Look for Plasmodium parasites.
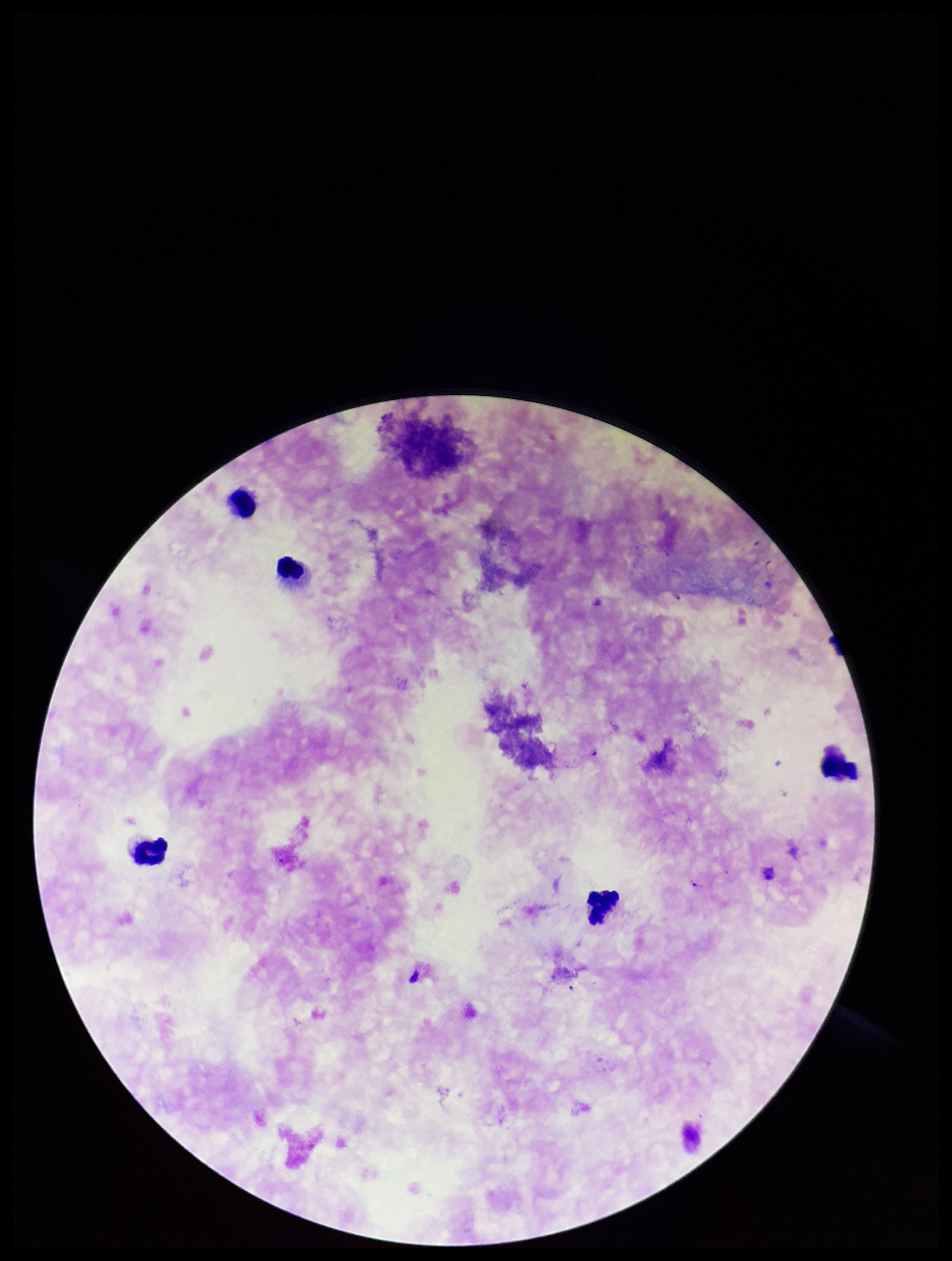
None detected.

Summary:
  - Species reported for this patient: Plasmodium falciparum
  - Parasite count: 0
  - Capture: smartphone photograph through the microscope eyepiece
  - Preparation: thick smear
  - Field of view: single
  - Stain: Giemsa
  - Image size: 952×1261 pixels
  - Patient malaria status: positive
  - Leukocyte count: 5